Comment on the morphology of the erythrocytes.
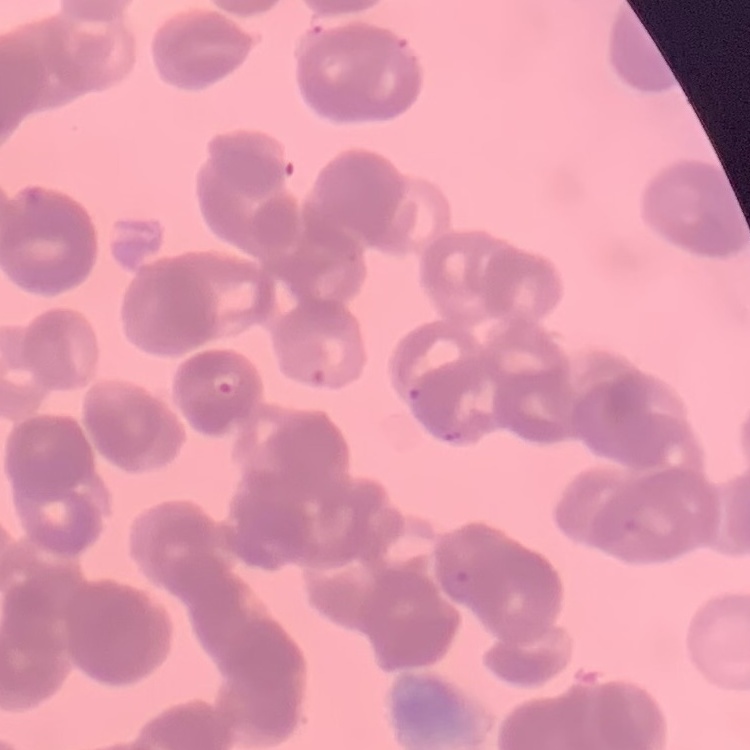

They show rouleaux formation.

preparation = thin blood film
stain = Field's or Giemsa
image type = one tile cut from a larger photomicrograph